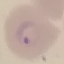
Malaria status: parasitized. Giemsa stain. Acquired by smartphone through the microscope eyepiece. Automatically extracted cell patch, resized to 64 × 64 pixels. Thin blood smear.